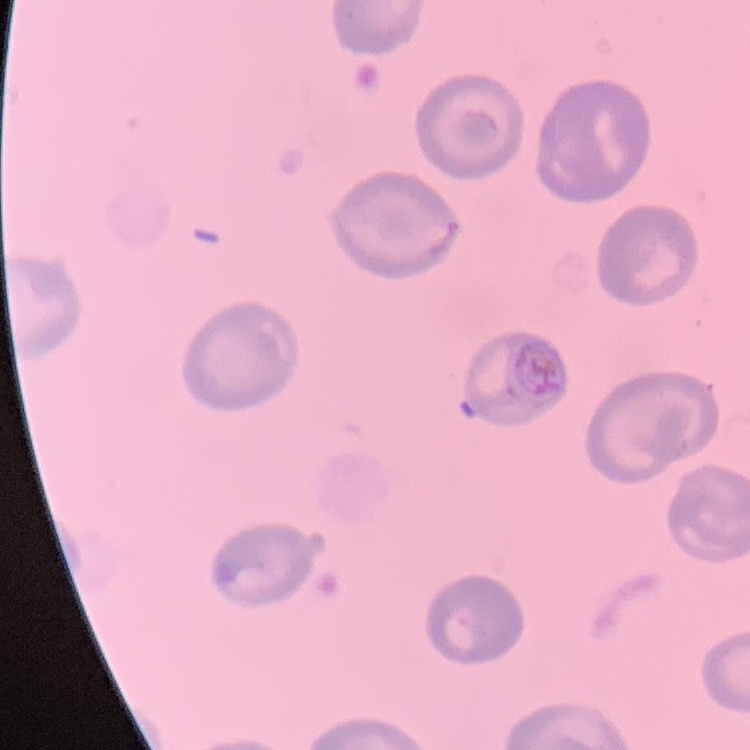

erythrocyte_morphology: no rouleaux formation
stain: Field's or Giemsa
image_type: square crop of a larger photomicrograph
preparation: thin peripheral smear